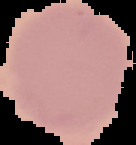
preparation = thin blood smear
result = negative for malaria parasites
image type = segmented cell region with the area outside set to black
image size = 136×145 pixels